Assess this cell for malaria.
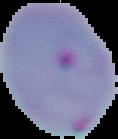
Parasitized.

From a thin blood film. The area outside the segmented cell region is set to black. Image is 118×139 pixels.